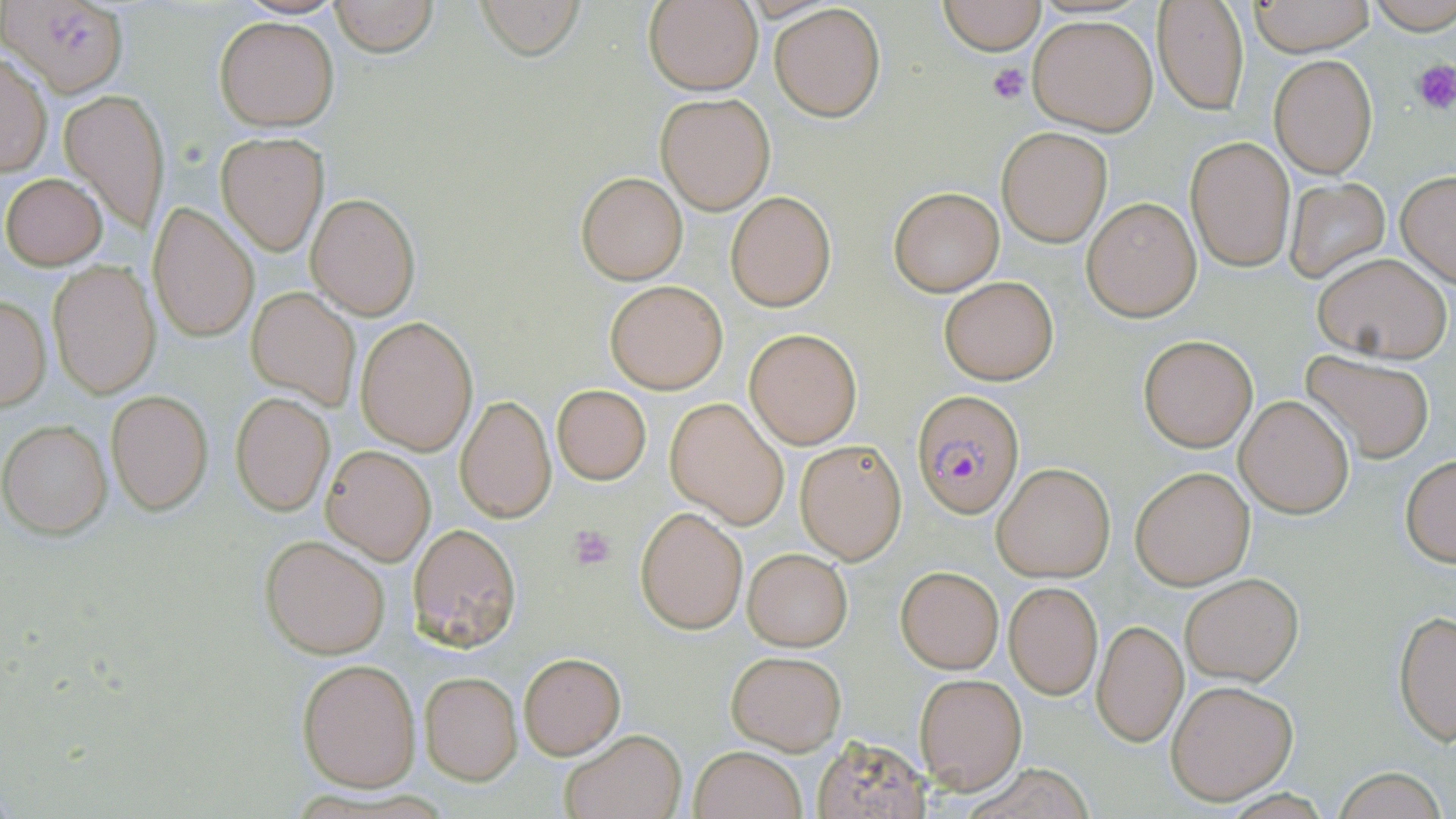
{
  "slide_level_diagnosis": "Plasmodium falciparum",
  "platelet_locations": "approximate bounding boxes as (x1,y1)-(x2,y2) corner pairs in pixels: (1411,59)-(1456,113), (987,63)-(1031,106), (569,525)-(616,571)",
  "stain": "May-Grünwald-Giemsa",
  "modality": "optical microscopy",
  "field_of_view": "one of a larger specimen",
  "uninfected_red_blood_cell_locations": "approximate bounding boxes as (x1,y1)-(x2,y2) corner pairs in pixels: (7,0)-(129,96), (329,0)-(438,56), (472,0)-(584,59), (645,0)-(762,95), (938,0)-(1047,53), (1249,1)-(1374,56), (1367,1)-(1456,35), (1152,2)-(1250,116), (770,4)-(887,121), (1028,14)-(1158,135), (215,17)-(338,130), (0,52)-(52,177), (1269,55)-(1376,178), (61,88)-(169,234), (656,93)-(775,214), (997,126)-(1112,246), (217,132)-(328,254), (1186,136)-(1295,272), (576,171)-(687,284), (3,172)-(105,268), (1396,172)-(1456,286), (1284,179)-(1391,282), (888,185)-(1004,295), (307,192)-(421,321), (726,192)-(835,310), (1082,196)-(1201,322), (148,201)-(259,343), (1311,251)-(1453,362), (47,259)-(160,400), (939,276)-(1058,385), (604,279)-(727,393), (246,287)-(360,411), (0,295)-(51,411), (355,316)-(477,453), (744,328)-(862,448), (1138,334)-(1257,452), (1302,350)-(1437,462), (550,384)-(651,484), (107,390)-(212,515), (230,393)-(335,515), (456,394)-(556,523), (1235,395)-(1356,519), (665,398)-(790,527), (1,420)-(113,538), (795,440)-(907,563), (322,445)-(435,563), (1401,454)-(1456,566), (991,463)-(1116,582), (1130,465)-(1257,591), (636,507)-(748,635), (408,523)-(521,650), (261,535)-(390,659), (743,548)-(853,651), (896,565)-(1003,673), (1180,572)-(1302,685), (1004,581)-(1103,700), (1393,608)-(1456,744), (1092,618)-(1188,747), (726,650)-(846,754), (518,652)-(625,760), (297,657)-(421,792), (419,672)-(523,785), (915,674)-(1028,794), (1166,678)-(1299,804), (559,730)-(685,819), (808,735)-(934,819), (689,746)-(808,819), (1331,767)-(1450,819)",
  "preparation": "thin blood film",
  "image_size": "1456×819 pixels",
  "magnification": "1000x",
  "plasmodium_falciparum_infected_red_blood_cell_locations": "approximate bounding boxes as (x1,y1)-(x2,y2) corner pairs in pixels: (913,391)-(1024,518)"
}